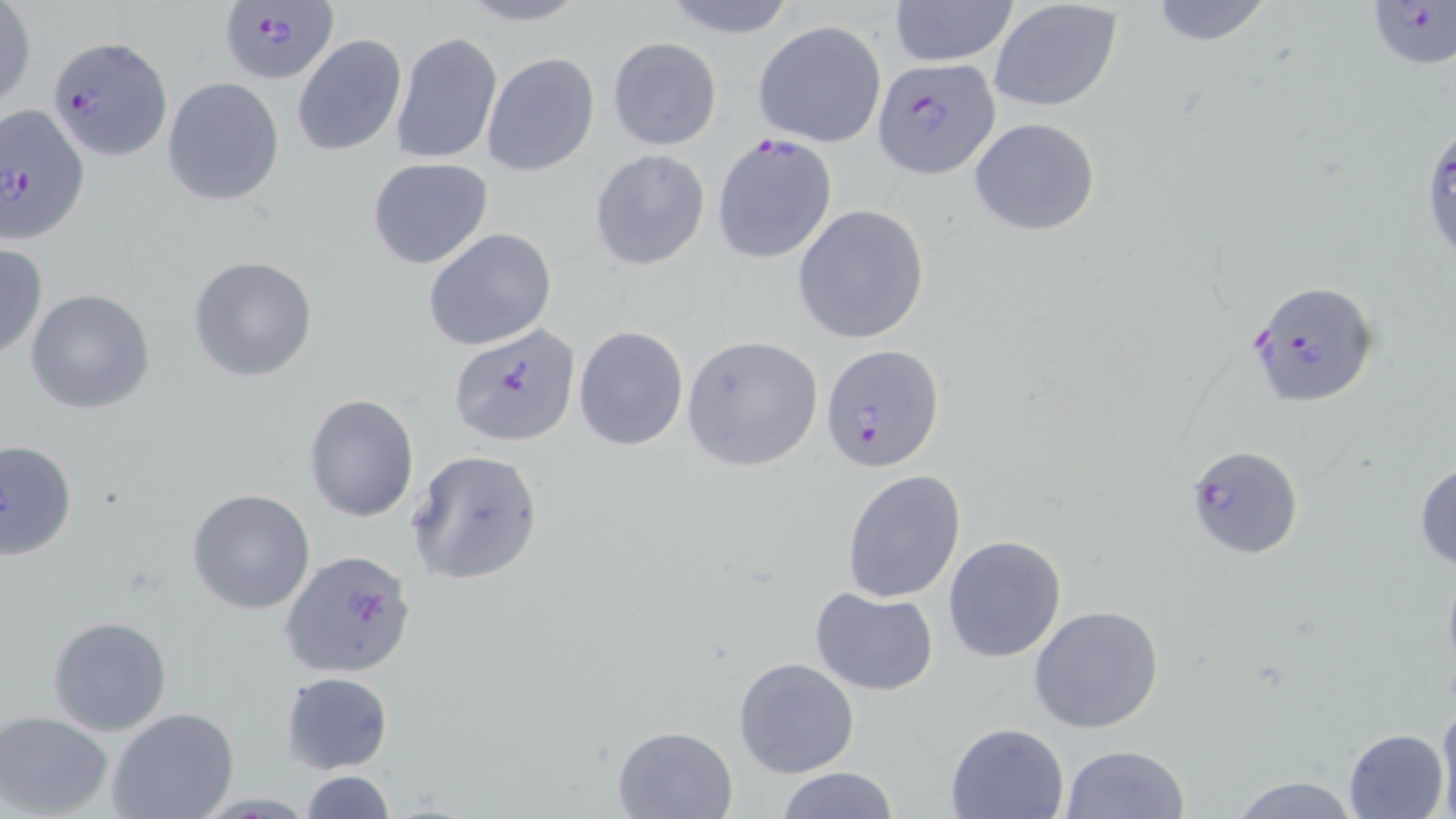 Approximate bounding boxes as named x1/y1/x2/y2 corners in pixels. Plasmodium falciparum-infected red blood cell locations: (x1=214, y1=0, x2=337, y2=85), (x1=1366, y1=1, x2=1456, y2=70), (x1=44, y1=32, x2=172, y2=164), (x1=873, y1=57, x2=999, y2=177), (x1=0, y1=102, x2=93, y2=245), (x1=1420, y1=112, x2=1455, y2=270), (x1=1247, y1=279, x2=1380, y2=409), (x1=449, y1=324, x2=581, y2=447), (x1=818, y1=343, x2=945, y2=473), (x1=1182, y1=443, x2=1304, y2=559), (x1=283, y1=547, x2=413, y2=680). Uninfected red blood cell locations: (x1=453, y1=0, x2=594, y2=28), (x1=656, y1=0, x2=801, y2=39), (x1=887, y1=0, x2=1019, y2=67), (x1=1143, y1=0, x2=1282, y2=49), (x1=988, y1=1, x2=1124, y2=112), (x1=1, y1=2, x2=36, y2=111), (x1=753, y1=19, x2=887, y2=148), (x1=391, y1=31, x2=502, y2=166), (x1=292, y1=34, x2=407, y2=156), (x1=607, y1=36, x2=722, y2=150), (x1=482, y1=53, x2=599, y2=176), (x1=163, y1=77, x2=285, y2=207), (x1=969, y1=118, x2=1101, y2=236), (x1=712, y1=134, x2=835, y2=263), (x1=589, y1=149, x2=710, y2=270), (x1=367, y1=158, x2=494, y2=269), (x1=389, y1=179, x2=530, y2=327), (x1=792, y1=205, x2=929, y2=343), (x1=425, y1=228, x2=556, y2=349), (x1=0, y1=244, x2=47, y2=359), (x1=187, y1=255, x2=318, y2=383), (x1=26, y1=288, x2=155, y2=414), (x1=572, y1=326, x2=688, y2=449), (x1=681, y1=334, x2=824, y2=471), (x1=304, y1=392, x2=418, y2=522), (x1=1, y1=439, x2=77, y2=561), (x1=407, y1=449, x2=544, y2=585), (x1=1414, y1=460, x2=1456, y2=572), (x1=842, y1=468, x2=966, y2=602), (x1=186, y1=489, x2=315, y2=614), (x1=943, y1=534, x2=1068, y2=663), (x1=809, y1=586, x2=940, y2=697), (x1=1027, y1=605, x2=1165, y2=735), (x1=47, y1=615, x2=172, y2=737), (x1=733, y1=656, x2=860, y2=777), (x1=280, y1=672, x2=394, y2=773), (x1=1436, y1=696, x2=1456, y2=818), (x1=106, y1=708, x2=240, y2=819), (x1=1, y1=711, x2=116, y2=819), (x1=946, y1=721, x2=1069, y2=817), (x1=612, y1=725, x2=737, y2=819), (x1=1344, y1=729, x2=1449, y2=818), (x1=1060, y1=745, x2=1189, y2=819), (x1=776, y1=767, x2=899, y2=819), (x1=298, y1=770, x2=399, y2=819), (x1=1226, y1=774, x2=1364, y2=817). Slide-level diagnosis: Plasmodium falciparum. Image is 1456×819 pixels. May-Grünwald-Giemsa stain. Single field of view. Optical microscopy. Captured at 1000x magnification. Thin blood film.